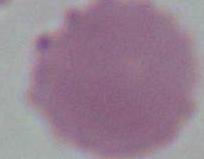

Summary:
  - Identification: erythrocyte
  - Magnification: 1000x
  - Modality: photomicrograph